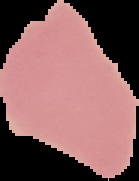
{
  "image_size": "139×181 pixels",
  "preparation": "thin blood smear",
  "image_type": "cell region segmented out of the field of view; surrounding area masked to black",
  "malaria_status": "uninfected"
}